Point out each malaria parasite.
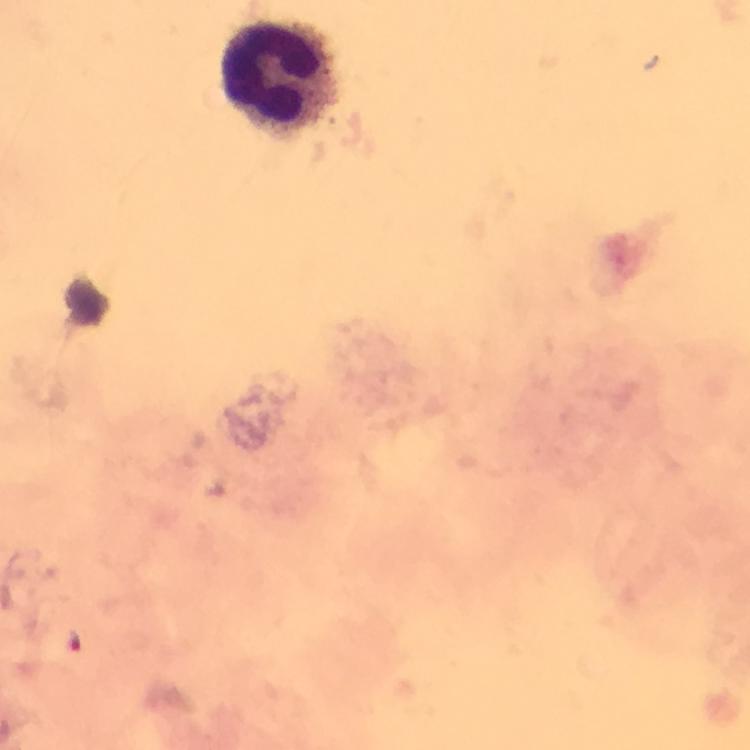

Approximate object centers, in pixels from the top-left corner.
Malaria parasites: (x=75, y=640).

Summary:
  - Leukocyte locations: (x=274, y=74)
  - Stain: Giemsa
  - Immersion oil: applied
  - Cropped from: a single field of view
  - Context: from a diagnostic examination for malaria
  - Capture: smartphone mounted on the microscope
  - Magnification: 100x
  - Image size: 750×750 pixels
  - Preparation: thick smear